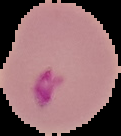
From a thin blood smear. Malaria status: parasitized. Image is 121×136 pixels. The area outside the segmented cell region is set to black.